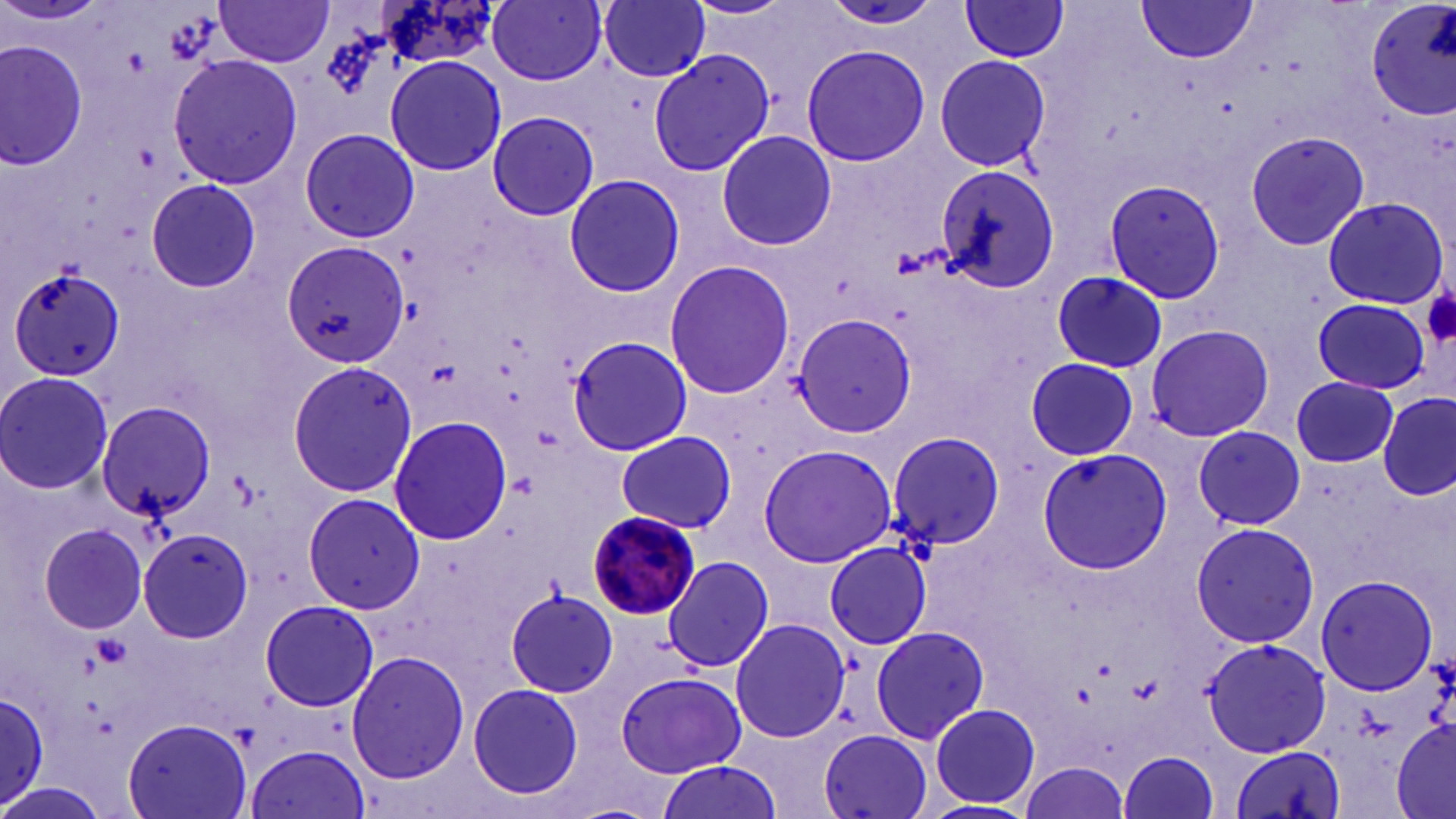 Approximate bounding boxes as named x1/y1/x2/y2 corners in pixels. Platelet locations: (x1=1421, y1=283, x2=1456, y2=348). Plasmodium malariae-infected red blood cell locations: (x1=586, y1=510, x2=703, y2=619). Uninfected red blood cell locations: (x1=215, y1=0, x2=334, y2=67), (x1=488, y1=0, x2=609, y2=84), (x1=599, y1=0, x2=713, y2=82), (x1=1365, y1=0, x2=1456, y2=122), (x1=819, y1=1, x2=948, y2=30), (x1=958, y1=1, x2=1073, y2=63), (x1=1133, y1=2, x2=1257, y2=64), (x1=1, y1=41, x2=87, y2=169), (x1=801, y1=43, x2=928, y2=168), (x1=648, y1=49, x2=774, y2=177), (x1=933, y1=53, x2=1051, y2=172), (x1=168, y1=54, x2=302, y2=190), (x1=384, y1=56, x2=506, y2=176), (x1=487, y1=112, x2=600, y2=221), (x1=295, y1=129, x2=416, y2=244), (x1=300, y1=129, x2=419, y2=242), (x1=1243, y1=130, x2=1371, y2=251), (x1=716, y1=131, x2=837, y2=250), (x1=937, y1=164, x2=1059, y2=294), (x1=563, y1=173, x2=687, y2=298), (x1=1103, y1=177, x2=1227, y2=305), (x1=146, y1=179, x2=261, y2=292), (x1=1104, y1=179, x2=1229, y2=303), (x1=1320, y1=196, x2=1448, y2=310), (x1=285, y1=240, x2=409, y2=368), (x1=662, y1=260, x2=797, y2=401), (x1=7, y1=266, x2=126, y2=384), (x1=1050, y1=271, x2=1167, y2=373), (x1=1309, y1=297, x2=1430, y2=394), (x1=793, y1=315, x2=918, y2=437), (x1=1145, y1=324, x2=1275, y2=442), (x1=566, y1=335, x2=694, y2=456), (x1=1025, y1=356, x2=1139, y2=460), (x1=287, y1=360, x2=417, y2=496), (x1=0, y1=371, x2=114, y2=496), (x1=1291, y1=375, x2=1397, y2=466), (x1=1377, y1=394, x2=1455, y2=500), (x1=95, y1=401, x2=218, y2=520), (x1=389, y1=416, x2=513, y2=543), (x1=1193, y1=426, x2=1305, y2=528), (x1=614, y1=431, x2=735, y2=533), (x1=884, y1=431, x2=1008, y2=551), (x1=888, y1=432, x2=1007, y2=552), (x1=758, y1=445, x2=899, y2=566), (x1=759, y1=445, x2=895, y2=568), (x1=1034, y1=446, x2=1173, y2=575), (x1=301, y1=494, x2=424, y2=613), (x1=32, y1=517, x2=152, y2=636), (x1=1189, y1=521, x2=1320, y2=648), (x1=138, y1=527, x2=254, y2=643), (x1=825, y1=542, x2=931, y2=649), (x1=664, y1=555, x2=772, y2=674), (x1=1316, y1=571, x2=1440, y2=697), (x1=505, y1=587, x2=618, y2=698), (x1=260, y1=598, x2=377, y2=712), (x1=729, y1=617, x2=851, y2=745), (x1=870, y1=625, x2=990, y2=745), (x1=1201, y1=638, x2=1330, y2=756), (x1=1200, y1=639, x2=1331, y2=762), (x1=346, y1=650, x2=469, y2=784), (x1=617, y1=670, x2=744, y2=778), (x1=467, y1=682, x2=585, y2=801), (x1=0, y1=685, x2=51, y2=810), (x1=929, y1=704, x2=1039, y2=811), (x1=123, y1=717, x2=252, y2=819), (x1=1391, y1=717, x2=1456, y2=817), (x1=816, y1=729, x2=935, y2=819), (x1=1229, y1=743, x2=1346, y2=817), (x1=245, y1=745, x2=370, y2=819), (x1=1121, y1=750, x2=1220, y2=818), (x1=653, y1=761, x2=779, y2=819), (x1=1015, y1=761, x2=1132, y2=819), (x1=0, y1=784, x2=106, y2=819). Slide-level diagnosis: Plasmodium malariae. One field of a larger specimen. Thin blood smear. Captured at 1000x magnification. Optical microscopy. Image is 1456×819 pixels. May-Grünwald-Giemsa-stained preparation.